Give the position of every malaria parasite and every leukocyte.
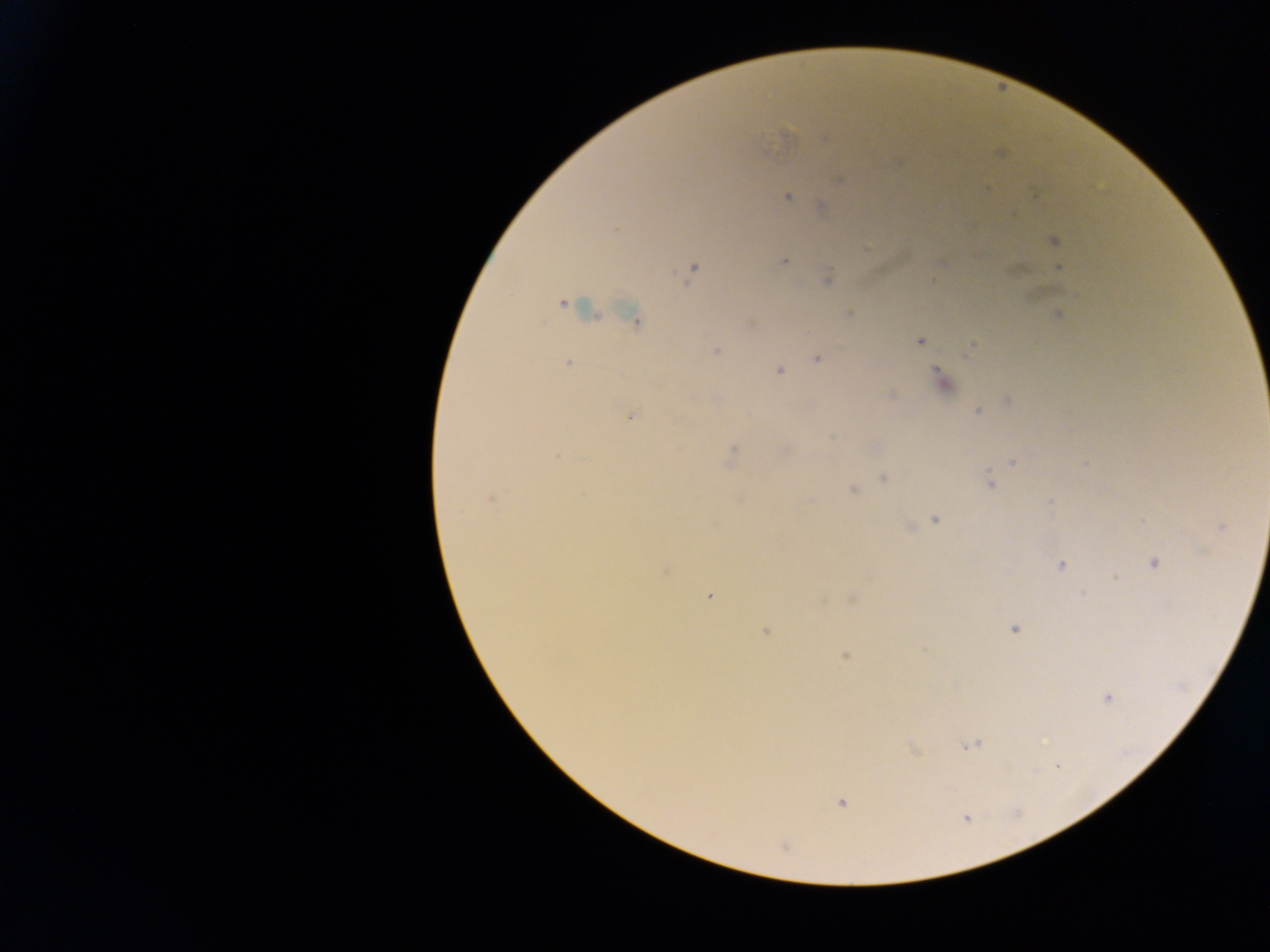
Approximate centers as x y in pixels.
Malaria parasites: 786 137; 826 140; 838 180; 987 189; 787 198; 823 207; 1054 241; 784 262; 1058 268; 693 269; 828 280; 562 304; 849 314; 1058 314; 634 319; 752 324; 919 342; 970 348; 717 350; 817 359; 567 364; 779 371; 942 380; 891 396; 1007 399; 978 411; 631 415; 730 457; 1013 461; 883 478; 990 484; 852 489; 490 499; 809 501; 1051 502; 935 518; 909 527; 1222 527; 1154 563; 1061 565; 664 571; 709 595; 1015 629; 766 632; 845 656; 1107 697; 972 746; 1059 766; 841 802; 966 818; 783 846.
No leukocytes observed.

Summary:
  - Capture: mobile-phone photograph through a microscope
  - Image size: 1270×952 pixels
  - Country: Ghana
  - Field of view: single
  - Preparation: thick blood film